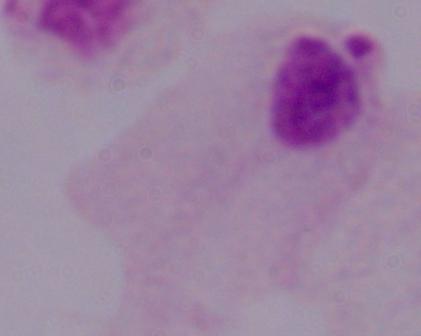
modality = photomicrograph
magnification = 1000x
identification = trichomonad